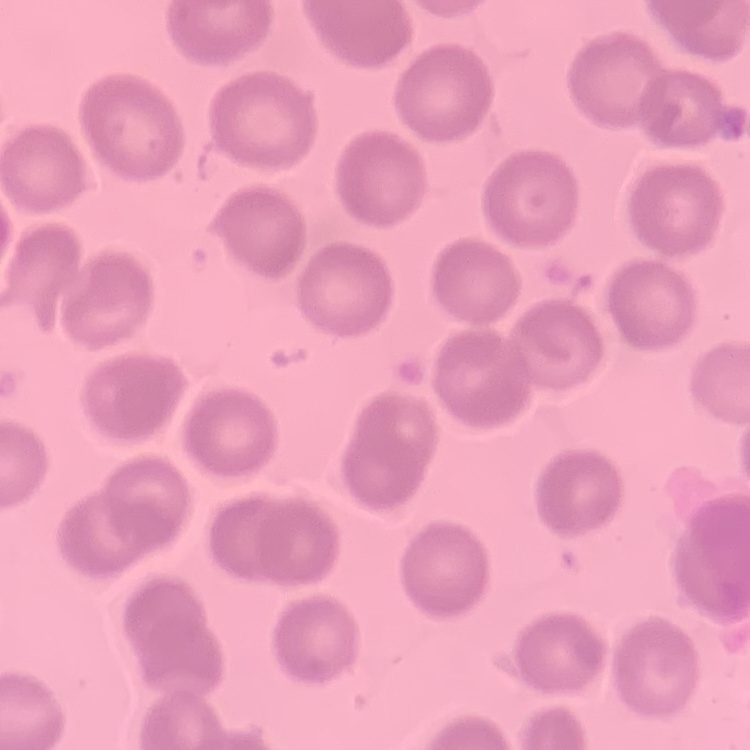
Summary:
  - Erythrocyte morphology: no rouleaux formation
  - Stain: Field's or Giemsa
  - Preparation: thin blood smear
  - Image type: one tile cut from a larger photomicrograph